Report the malaria status of this cell.
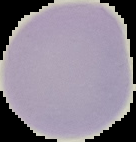
Uninfected.

Image is 136×142 pixels. Cell region segmented out of the field of view; the surrounding area is masked to black. From a thin blood smear.